Point out each Plasmodium parasite.
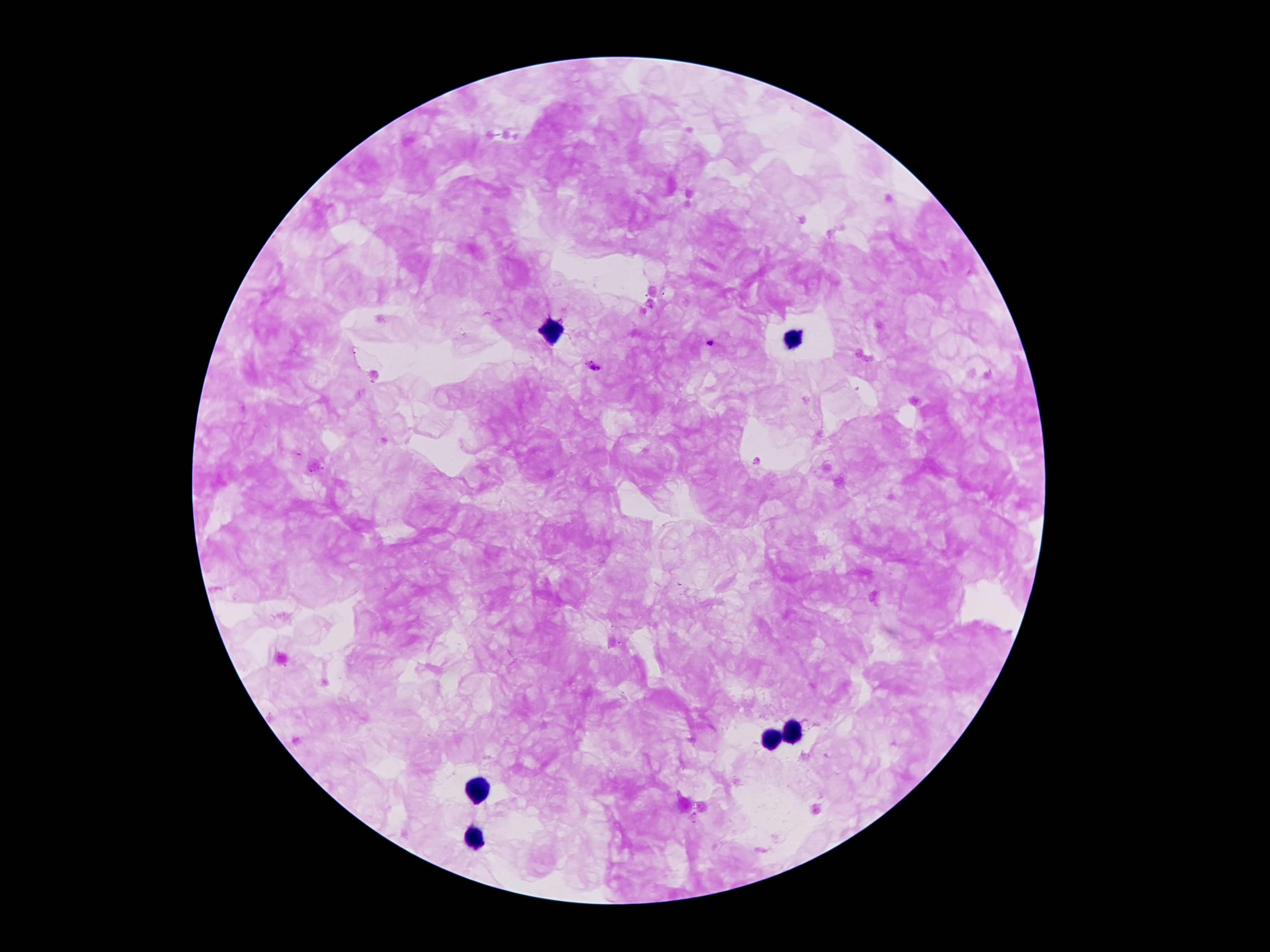

Approximate centers as {x, y} in pixels.
Plasmodium parasites: {708, 343}, {593, 368}.

Summary:
  - Leukocyte locations: {551, 330}, {796, 341}, {789, 735}, {770, 740}, {476, 789}, {474, 837}
  - Preparation: thick blood smear
  - Field of view: single
  - Magnification: 100x
  - Capture: smartphone through the microscope eyepiece
  - Stain: Giemsa
  - Image size: 1270×952 pixels
  - Patient malaria status: infected with Plasmodium falciparum